Identify the cell.
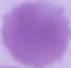
This is an erythrocyte.

modality: micrograph
magnification: 1000x